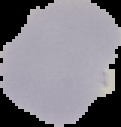
image type = segmented cell region with the area outside set to black
result = no malaria parasites seen
preparation = thin blood smear
image size = 121×127 pixels